Name the parasite shown.
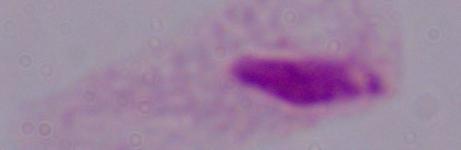
This is a trichomonad.

Summary:
  - Modality: photomicrograph
  - Magnification: 1000x